Find each parasitized red blood cell.
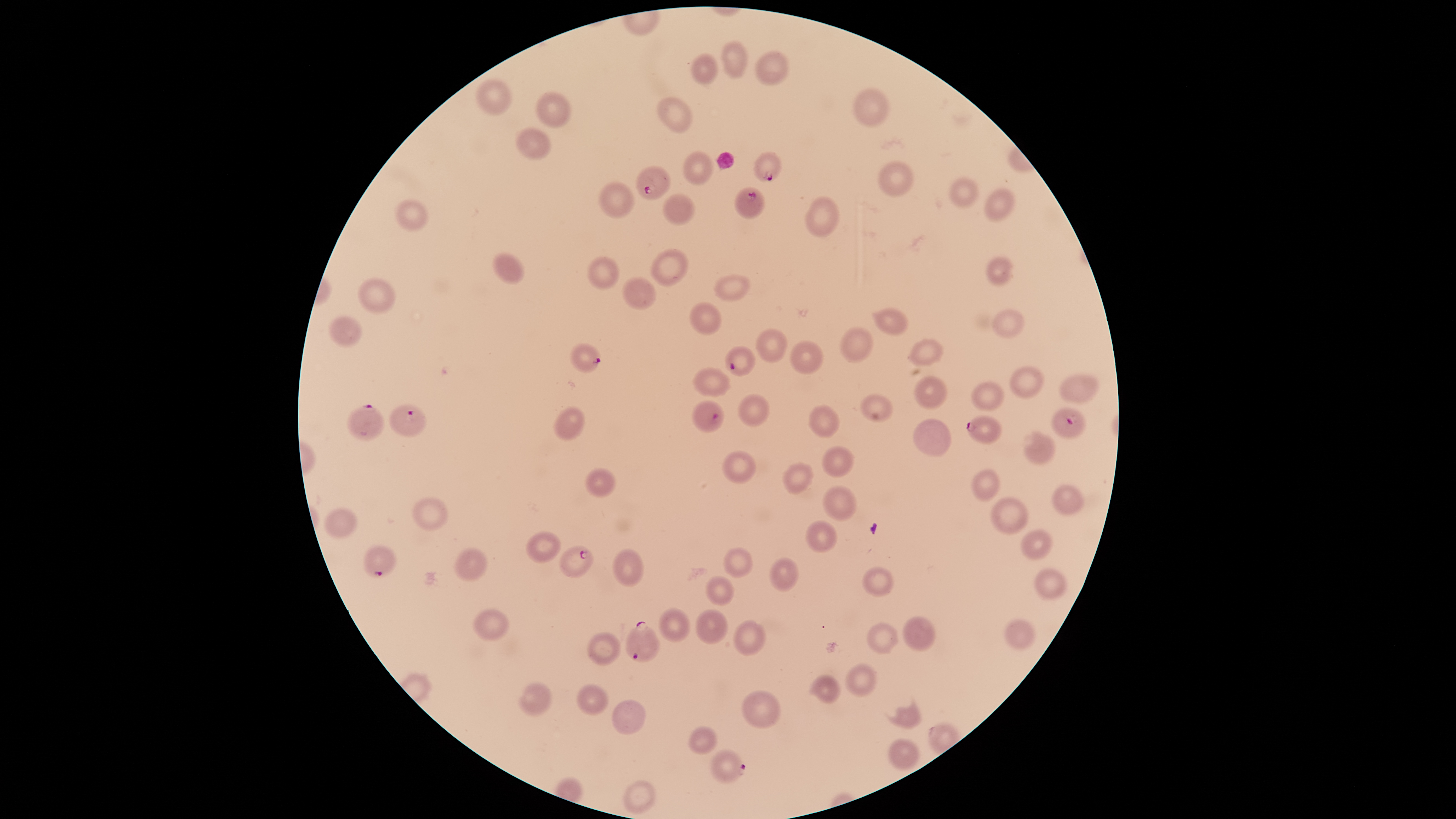
Approximate bounding boxes as {left, top, right, bottom} in pixels.
Parasitized red blood cells: {753, 151, 782, 183}, {635, 165, 670, 201}, {734, 186, 764, 219}, {569, 343, 600, 373}, {724, 345, 756, 376}, {692, 399, 724, 433}, {346, 404, 385, 442}, {389, 404, 426, 437}, {1051, 408, 1086, 440}, {966, 415, 1001, 444}, {364, 545, 397, 578}, {559, 545, 593, 578}, {625, 621, 660, 662}, {710, 750, 746, 784}.

Approximate bounding boxes as {left, top, right, bottom} in pixels. Uninfected red blood cells: {722, 40, 748, 78}, {755, 51, 789, 85}, {691, 54, 719, 84}, {477, 79, 512, 115}, {854, 88, 889, 126}, {537, 91, 571, 128}, {657, 96, 692, 133}, {516, 126, 551, 158}, {683, 151, 713, 185}, {877, 160, 913, 197}, {947, 176, 978, 208}, {599, 181, 635, 218}, {984, 188, 1014, 222}, {663, 194, 695, 225}, {805, 196, 838, 237}, {394, 200, 428, 231}, {650, 249, 688, 287}, {492, 252, 525, 284}, {587, 256, 619, 289}, {986, 256, 1013, 285}, {714, 274, 751, 302}, {622, 276, 656, 310}, {358, 278, 395, 314}, {690, 302, 722, 335}, {872, 308, 909, 335}, {992, 309, 1024, 338}, {329, 315, 360, 348}, {839, 326, 873, 362}, {755, 328, 787, 362}, {909, 338, 943, 365}, {789, 341, 823, 374}, {1010, 366, 1044, 398}, {693, 368, 729, 397}, {1060, 375, 1099, 402}, {914, 376, 947, 409}, {972, 381, 1004, 411}, {739, 394, 769, 427}, {861, 394, 893, 422}, {807, 404, 840, 439}, {555, 406, 584, 441}, {912, 420, 951, 456}, {1022, 431, 1056, 464}, {821, 446, 854, 478}, {722, 450, 756, 483}, {783, 463, 813, 495}, {585, 468, 614, 498}, {971, 469, 999, 501}, {1051, 484, 1084, 515}, {823, 485, 855, 520}, {412, 497, 448, 532}, {990, 497, 1029, 535}, {325, 508, 357, 538}, {805, 520, 837, 553}, {1020, 529, 1052, 559}, {526, 531, 560, 564}, {723, 547, 753, 578}, {455, 548, 486, 581}, {613, 549, 643, 587}, {769, 557, 799, 592}, {863, 567, 893, 596}, {1034, 568, 1067, 600}, {704, 575, 733, 606}, {473, 608, 507, 640}, {659, 608, 690, 643}, {696, 609, 728, 645}, {903, 616, 936, 651}, {1004, 618, 1034, 650}, {734, 621, 764, 656}, {867, 623, 897, 654}, {588, 631, 619, 666}, {846, 664, 875, 697}, {813, 676, 840, 704}, {518, 682, 551, 718}, {577, 684, 608, 716}, {742, 690, 779, 729}, {613, 700, 645, 736}, {897, 706, 920, 730}, {689, 727, 715, 755}, {889, 738, 918, 771}, {624, 781, 655, 814}. Photographed with a smartphone camera through the microscope eyepiece. Giemsa stain. One field of view of the specimen. Species: Plasmodium falciparum. Image is 1456×819 pixels. Thin blood smear. The visible region is circular.